Report the malaria status of this cell.
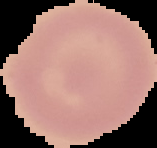

Uninfected.

Image is 157×148 pixels. From a thin blood smear. Segmented cell region on a black background.